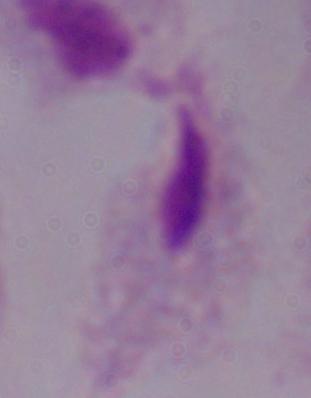

magnification = 1000x
modality = micrograph
identification = trichomonad